Locate every Plasmodium parasite by life-cycle stage, and every leukocyte.
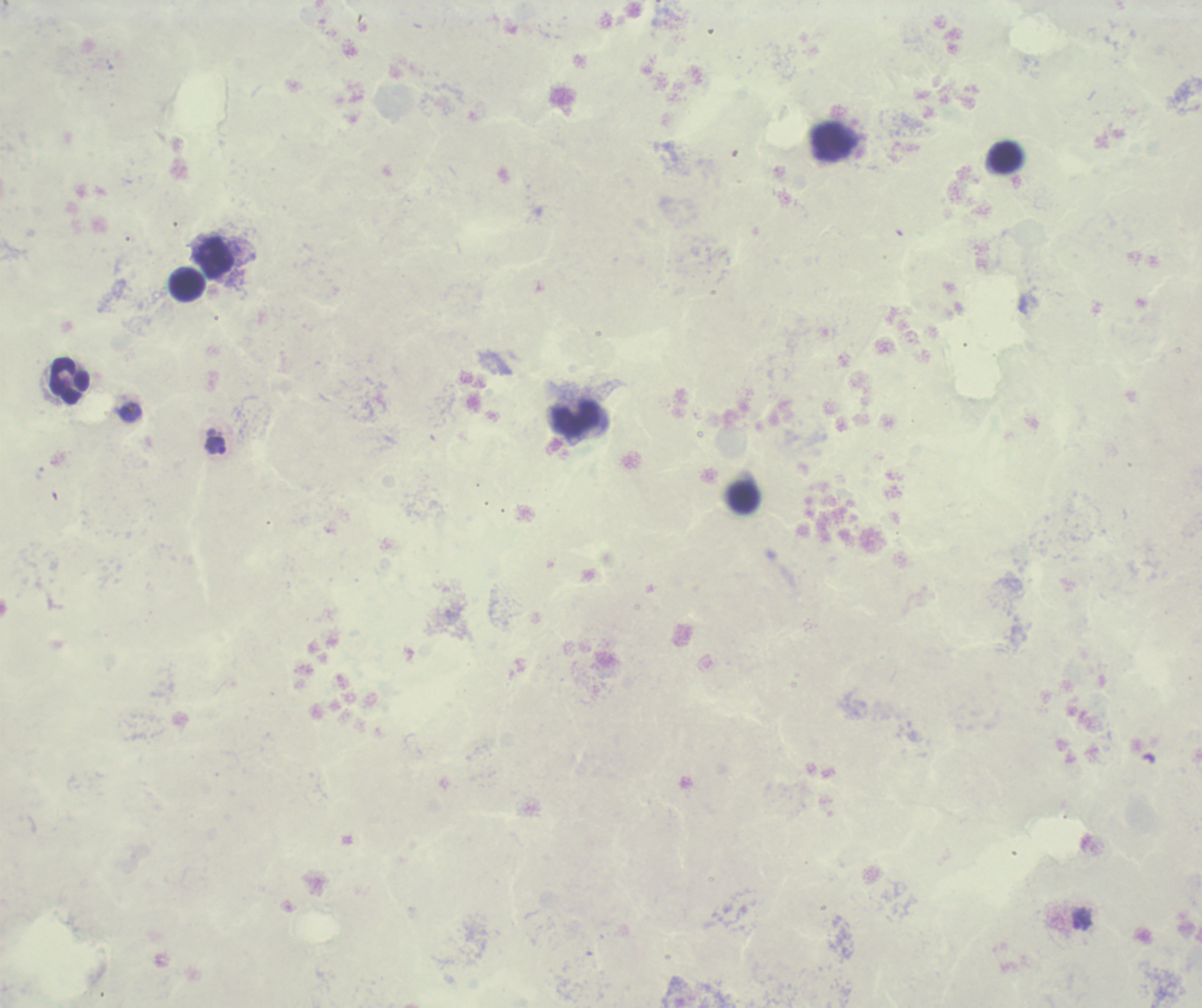
Approximate object centers, in pixels from the top-left corner.
Trophozoites: (x=215, y=445), (x=1083, y=918).
No schizont or gametocyte forms observed.
Leukocytes: (x=834, y=142), (x=1006, y=158), (x=214, y=258), (x=188, y=285), (x=69, y=380), (x=576, y=419).

{
  "magnification": "100x",
  "coloration_quality": "bad",
  "context": "previously used in a real diagnosis",
  "preparation": "thick blood film",
  "image_size": "1202×1008 pixels",
  "background_quality": "poor",
  "field_of_view": "one from this slide",
  "stain": "Romanowsky"
}